Report the malaria status of this cell.
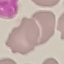

Uninfected.

Summary:
  - Capture: smartphone through the microscope eyepiece
  - Stain: Giemsa
  - Image type: cell patch, automatically extracted from a larger field of view and resized to 64 × 64 pixels
  - Preparation: thin smear